Identify the parasite.
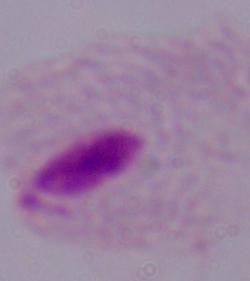

This is a trichomonad.

Micrograph. 1000x magnification.